Report the malaria status of this cell.
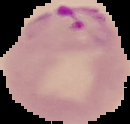
It is parasitized.

image type = segmented cell region on a black background
image size = 130×124 pixels
preparation = thin blood smear